Assess this cell for malaria.
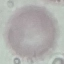

Uninfected.

Summary:
  - Stain: Giemsa
  - Preparation: thin blood film
  - Capture: smartphone through the microscope eyepiece
  - Image type: automatically extracted cell patch, resized to 64 × 64 pixels